Comment on the morphology of the erythrocytes.
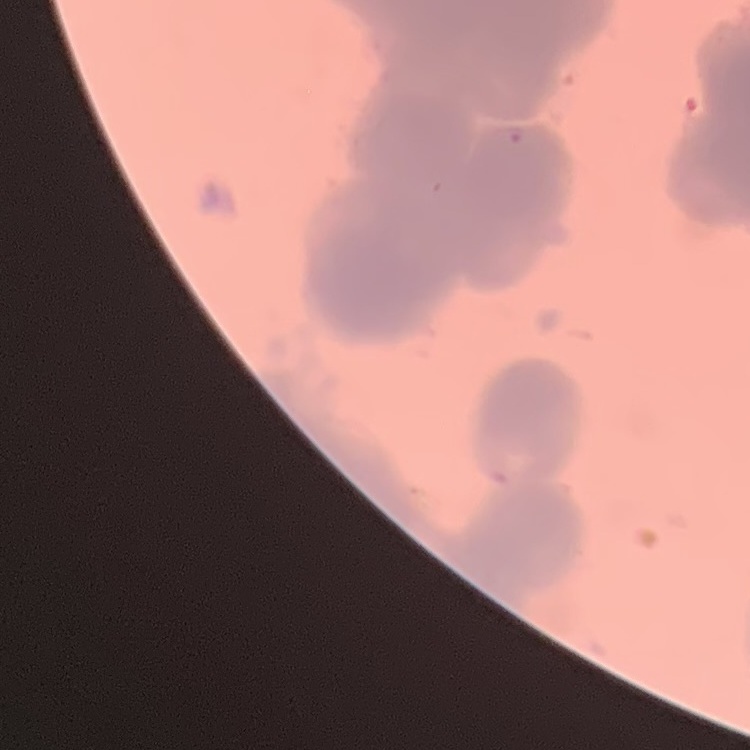
Rouleaux formation.

stain = Field's or Giemsa
image type = square crop of a larger photomicrograph
preparation = thin blood smear